Locate every Plasmodium ovale-infected red blood cell.
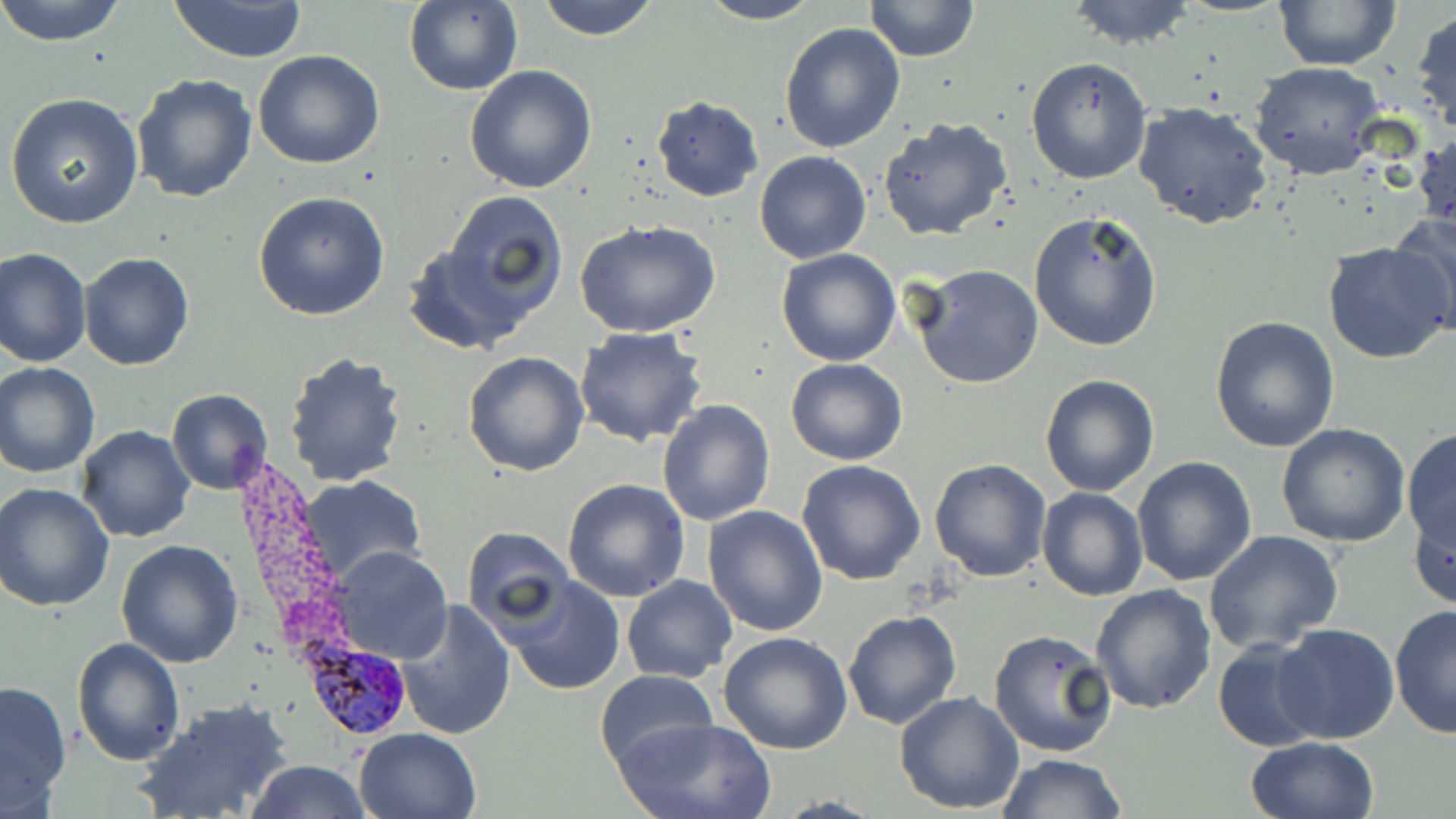

Approximate bounding boxes as named x1/y1/x2/y2 corners in pixels.
Plasmodium ovale-infected red blood cells: (x1=300, y1=639, x2=412, y2=742).

slide_level_diagnosis: Plasmodium ovale
preparation: thin blood smear
modality: light microscopy
image_size: 1456×819 pixels
uninfected_red_blood_cell_locations: 'approximate bounding boxes as named x1/y1/x2/y2 corners in pixels: (x1=0, y1=0, x2=128, y2=46), (x1=165, y1=0, x2=310, y2=64), (x1=534, y1=0, x2=661, y2=41), (x1=694, y1=0, x2=826, y2=25), (x1=864, y1=0, x2=981, y2=62), (x1=1063, y1=0, x2=1200, y2=50), (x1=404, y1=1, x2=524, y2=97), (x1=1275, y1=1, x2=1400, y2=71), (x1=1410, y1=8, x2=1456, y2=139), (x1=779, y1=21, x2=906, y2=154), (x1=252, y1=49, x2=386, y2=169), (x1=1025, y1=57, x2=1152, y2=186), (x1=1248, y1=61, x2=1385, y2=179), (x1=465, y1=64, x2=598, y2=193), (x1=131, y1=74, x2=258, y2=205), (x1=5, y1=93, x2=145, y2=230), (x1=651, y1=96, x2=764, y2=201), (x1=1133, y1=101, x2=1276, y2=232), (x1=877, y1=119, x2=1014, y2=242), (x1=1413, y1=127, x2=1455, y2=243), (x1=754, y1=151, x2=870, y2=263), (x1=443, y1=190, x2=569, y2=311), (x1=252, y1=191, x2=390, y2=322), (x1=1028, y1=210, x2=1165, y2=352), (x1=1389, y1=210, x2=1456, y2=334), (x1=575, y1=219, x2=721, y2=338), (x1=401, y1=237, x2=544, y2=353), (x1=1323, y1=242, x2=1455, y2=364), (x1=1, y1=247, x2=91, y2=367), (x1=776, y1=248, x2=902, y2=367), (x1=78, y1=251, x2=194, y2=371), (x1=910, y1=263, x2=1043, y2=390), (x1=1209, y1=315, x2=1340, y2=452), (x1=573, y1=327, x2=708, y2=447), (x1=283, y1=350, x2=410, y2=488), (x1=463, y1=350, x2=590, y2=477), (x1=787, y1=358, x2=908, y2=467), (x1=0, y1=362, x2=100, y2=476), (x1=1040, y1=375, x2=1158, y2=496), (x1=167, y1=388, x2=274, y2=494), (x1=657, y1=399, x2=776, y2=525), (x1=1276, y1=423, x2=1411, y2=548), (x1=76, y1=425, x2=196, y2=544), (x1=1403, y1=429, x2=1456, y2=555), (x1=1132, y1=456, x2=1257, y2=587), (x1=930, y1=458, x2=1053, y2=582), (x1=796, y1=460, x2=925, y2=586), (x1=297, y1=475, x2=426, y2=588), (x1=562, y1=480, x2=691, y2=603), (x1=2, y1=483, x2=117, y2=613), (x1=1037, y1=487, x2=1147, y2=601), (x1=1410, y1=501, x2=1456, y2=613), (x1=703, y1=505, x2=829, y2=637), (x1=462, y1=527, x2=575, y2=631), (x1=1202, y1=530, x2=1344, y2=654), (x1=114, y1=539, x2=244, y2=667), (x1=329, y1=548, x2=451, y2=664), (x1=622, y1=575, x2=738, y2=684), (x1=503, y1=576, x2=627, y2=696), (x1=1090, y1=586, x2=1217, y2=716), (x1=396, y1=600, x2=516, y2=740), (x1=1390, y1=602, x2=1456, y2=741), (x1=843, y1=611, x2=962, y2=730), (x1=1272, y1=624, x2=1400, y2=745), (x1=987, y1=628, x2=1119, y2=760), (x1=720, y1=630, x2=854, y2=754), (x1=1213, y1=636, x2=1326, y2=753), (x1=72, y1=637, x2=185, y2=766), (x1=595, y1=670, x2=718, y2=774), (x1=0, y1=680, x2=72, y2=812), (x1=895, y1=691, x2=1025, y2=813), (x1=135, y1=698, x2=294, y2=819), (x1=614, y1=716, x2=776, y2=818), (x1=353, y1=727, x2=481, y2=818), (x1=1245, y1=736, x2=1381, y2=819), (x1=998, y1=753, x2=1129, y2=818), (x1=247, y1=759, x2=371, y2=818)'
stain: May-Grünwald-Giemsa
magnification: 1000x
field_of_view: single